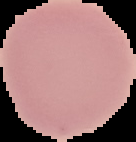 From a thin blood smear. Result: no Plasmodium parasites detected. The area outside the segmented cell region is set to black. Image is 136×142 pixels.